Identify the parasite.
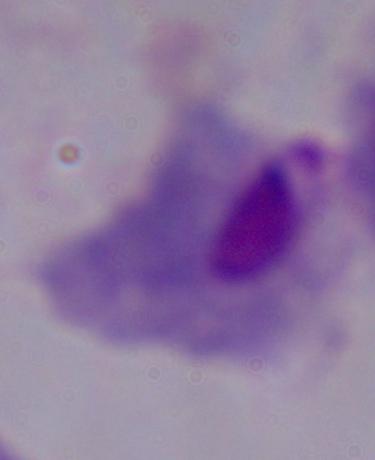

This is a trichomonad.

1000x magnification. Photomicrograph.